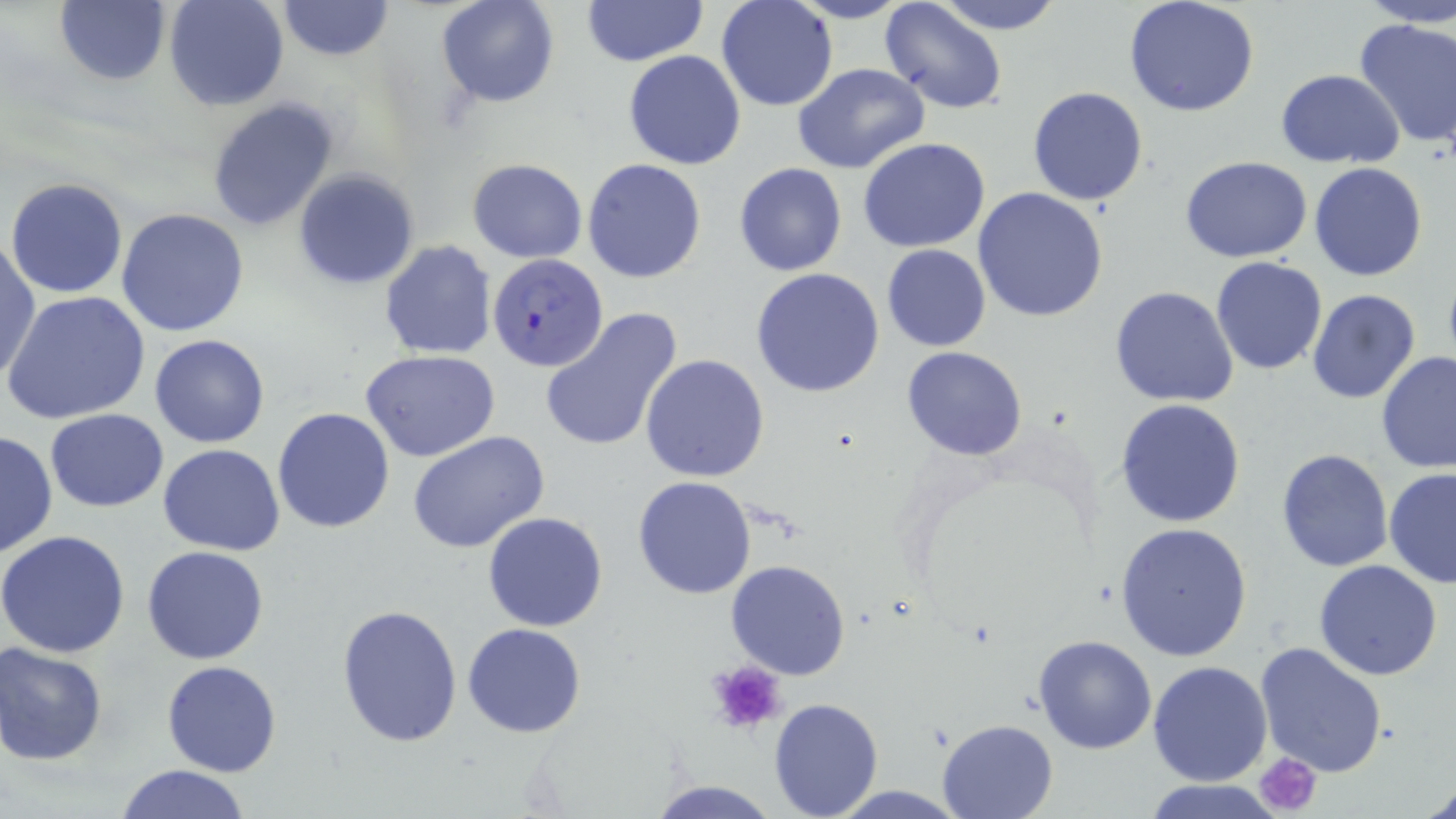

Summary:
  - Coordinate format: approximate bounding boxes as [x1, y1, x2, y2] in pixels
  - Uninfected red blood cell locations: [55, 0, 170, 86], [162, 0, 290, 112], [274, 0, 396, 62], [436, 0, 560, 108], [582, 0, 709, 67], [715, 0, 838, 112], [787, 0, 914, 25], [932, 0, 1067, 35], [1121, 0, 1262, 118], [1354, 0, 1455, 27], [877, 2, 1009, 116], [1353, 16, 1456, 150], [623, 50, 746, 169], [791, 62, 930, 174], [1275, 69, 1405, 166], [1026, 86, 1147, 207], [207, 98, 339, 232], [859, 137, 991, 253], [1180, 157, 1313, 262], [468, 158, 587, 264], [582, 158, 707, 283], [734, 161, 847, 277], [1308, 162, 1429, 281], [293, 168, 420, 290], [6, 177, 128, 299], [974, 186, 1109, 322], [116, 207, 251, 338], [1, 237, 40, 383], [380, 241, 497, 358], [881, 244, 990, 351], [1210, 256, 1327, 375], [751, 267, 886, 397], [1109, 285, 1239, 407], [1305, 289, 1422, 405], [2, 290, 151, 425], [540, 308, 683, 454], [150, 334, 271, 448], [902, 347, 1029, 461], [360, 349, 501, 461], [1376, 351, 1456, 475], [641, 353, 769, 483], [1115, 399, 1246, 527], [271, 407, 396, 533], [44, 409, 169, 512], [1, 429, 57, 561], [407, 430, 552, 554], [158, 443, 284, 555], [1275, 447, 1394, 573], [1384, 469, 1456, 589], [632, 475, 757, 599], [482, 511, 609, 632], [1115, 523, 1252, 661], [0, 531, 130, 658], [141, 546, 269, 664], [725, 559, 852, 680], [1313, 560, 1443, 681], [335, 601, 463, 746], [462, 623, 587, 737], [1032, 635, 1159, 754], [1254, 640, 1389, 778], [0, 642, 108, 765], [161, 660, 282, 777], [1148, 661, 1272, 785], [769, 698, 884, 818], [937, 719, 1056, 818], [113, 764, 253, 819], [647, 779, 780, 818], [1144, 779, 1285, 818], [1421, 780, 1456, 819]
  - Plasmodium falciparum-infected red blood cell locations: [488, 252, 609, 371]
  - Platelet locations: [706, 657, 788, 736], [1255, 751, 1323, 816]
  - Slide-level diagnosis: Plasmodium falciparum
  - Field of view: single
  - Image size: 1456×819 pixels
  - Stain: May-Grünwald-Giemsa
  - Modality: optical microscopy
  - Preparation: thin blood film
  - Magnification: 1000x